Describe the morphology of the red blood cells.
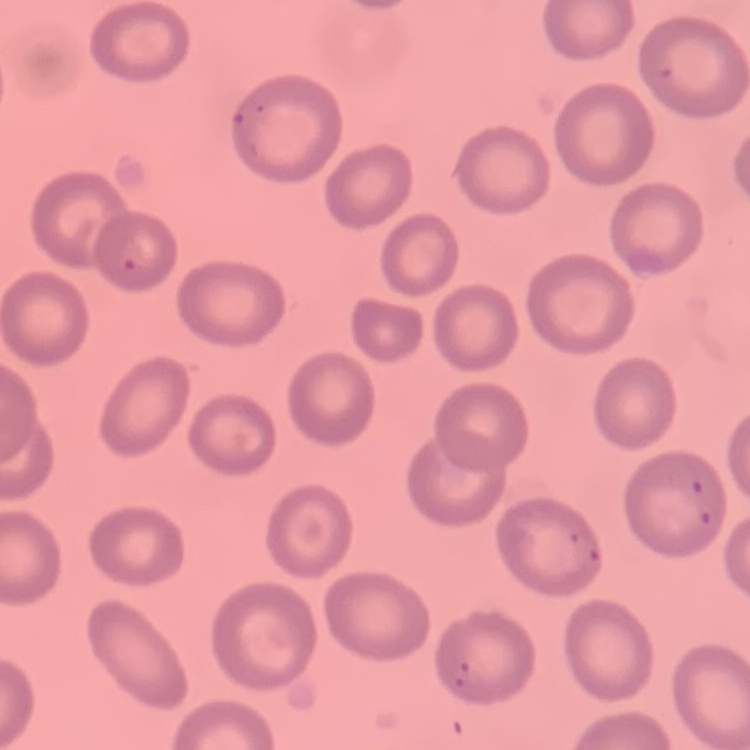
They show no rouleaux formation.

Field's or Giemsa stain. One tile cut from a larger photomicrograph. Thin blood smear.